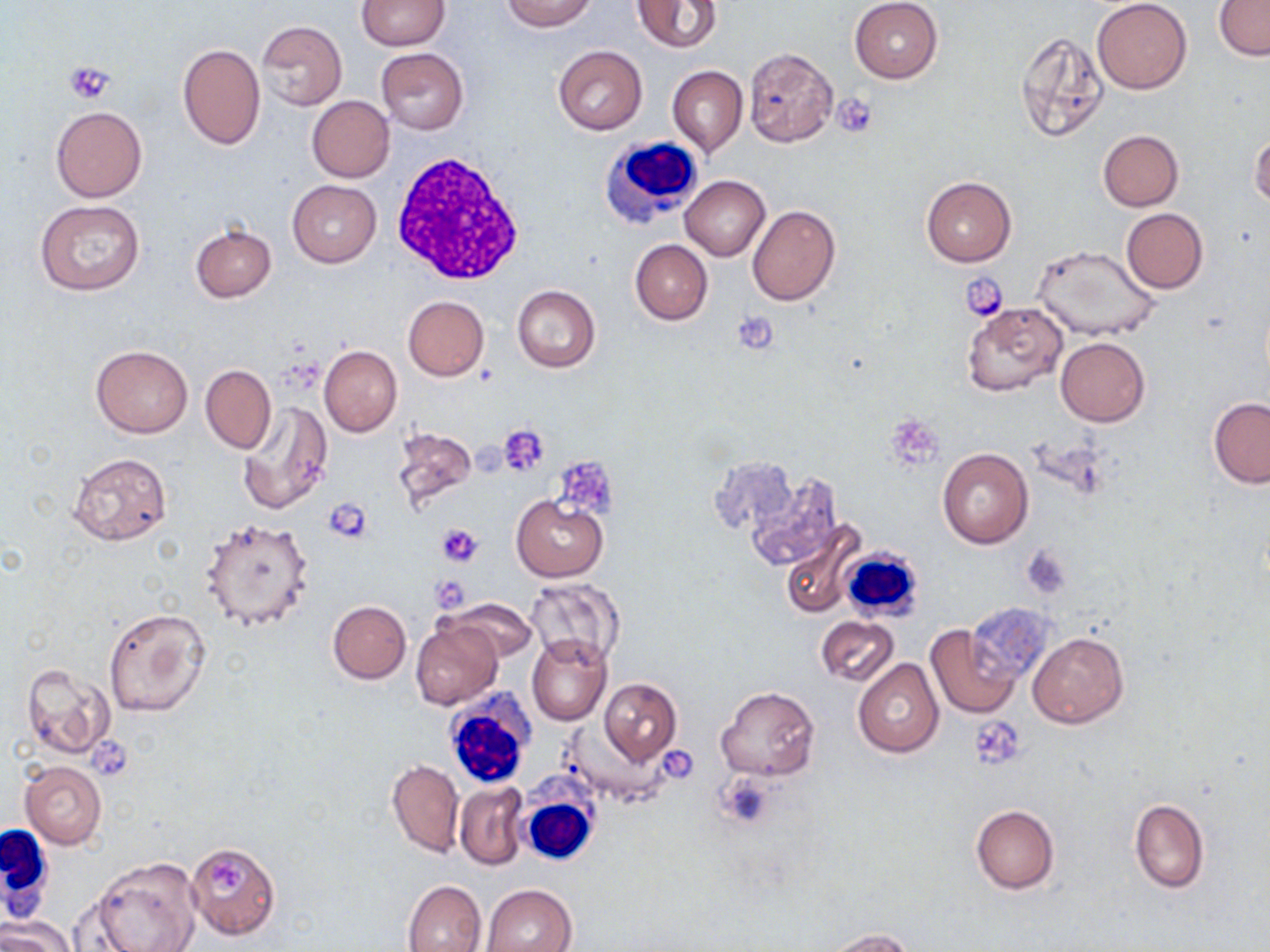
Approximate bounding boxes as (x1, y1, x2, y2) in pixels. White blood cell locations: (602, 135, 705, 223), (390, 155, 524, 284), (837, 545, 928, 625), (445, 689, 535, 792), (519, 788, 601, 865), (1, 821, 54, 924). Platelet locations: (64, 62, 116, 105), (832, 93, 876, 137), (962, 273, 1009, 321), (732, 309, 781, 355), (498, 424, 550, 478), (560, 457, 623, 515), (324, 499, 373, 543), (435, 523, 484, 568), (1022, 545, 1073, 601), (970, 717, 1025, 770), (88, 738, 131, 779). Uninfected red blood cell locations: (356, 0, 450, 50), (500, 0, 597, 31), (849, 0, 943, 83), (1092, 0, 1192, 93), (1215, 0, 1270, 60), (632, 1, 722, 53), (257, 20, 346, 109), (1017, 32, 1110, 142), (177, 42, 266, 151), (552, 45, 647, 134), (376, 48, 469, 134), (744, 48, 838, 147), (667, 65, 748, 157), (307, 95, 394, 182), (51, 106, 147, 202), (1097, 130, 1183, 211), (1249, 130, 1270, 209), (681, 176, 770, 260), (921, 176, 1017, 267), (287, 180, 381, 266), (35, 201, 144, 297), (748, 204, 840, 305), (1120, 208, 1207, 293), (191, 225, 276, 302), (630, 240, 712, 324), (1034, 245, 1160, 342), (512, 285, 601, 372), (403, 296, 489, 380), (962, 302, 1068, 395), (1056, 337, 1150, 426), (91, 345, 193, 438), (319, 345, 402, 437), (201, 364, 275, 454), (1208, 397, 1270, 488), (237, 401, 332, 515), (389, 425, 479, 515), (938, 448, 1034, 548), (67, 452, 172, 546), (708, 456, 800, 537), (745, 470, 845, 572), (511, 495, 607, 582), (201, 517, 315, 631), (780, 524, 862, 618), (525, 578, 625, 665), (444, 596, 538, 663), (328, 600, 411, 683), (964, 602, 1058, 687), (101, 606, 210, 718), (815, 614, 899, 688), (411, 621, 502, 709), (924, 623, 1022, 719), (1028, 631, 1128, 729), (527, 635, 612, 725), (852, 658, 943, 757), (19, 661, 115, 759), (598, 678, 681, 764), (716, 685, 821, 780), (561, 722, 666, 807), (387, 758, 463, 858), (19, 761, 106, 849), (454, 781, 528, 870), (1129, 799, 1209, 893), (971, 805, 1059, 894), (186, 841, 280, 938), (90, 856, 202, 952), (403, 879, 486, 952), (481, 883, 576, 952), (0, 916, 73, 952), (818, 928, 917, 951). Slide-level diagnosis: no evidence of blood parasites. Captured at 1000x magnification. Thin blood smear. May-Grünwald-Giemsa-stained preparation. One field of a larger specimen. Image is 1270×952 pixels. Optical microscopy.